Name the parasite shown.
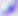
This is Toxoplasma gondii.

{
  "magnification": "400x",
  "modality": "photomicrograph"
}